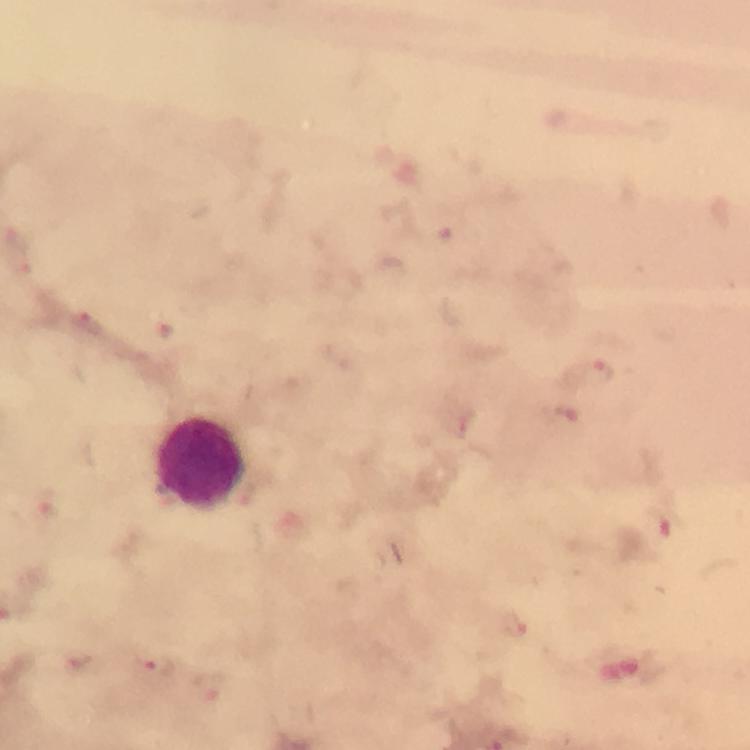

Approximate centers as (x, y) in pixels.
Summary:
  - Leukocyte locations: (203, 465)
  - Plasmodium parasite locations: (87, 326), (166, 331), (586, 373), (563, 416), (658, 524), (79, 667), (160, 668)
  - Context: from a malaria diagnostic workup
  - Magnification: 100x
  - Immersion oil: used
  - Preparation: thick blood smear
  - Cropped from: one field of view
  - Stain: Giemsa
  - Capture: smartphone mounted on the microscope
  - Image size: 750×750 pixels